Outline each Plasmodium ovale-infected red blood cell.
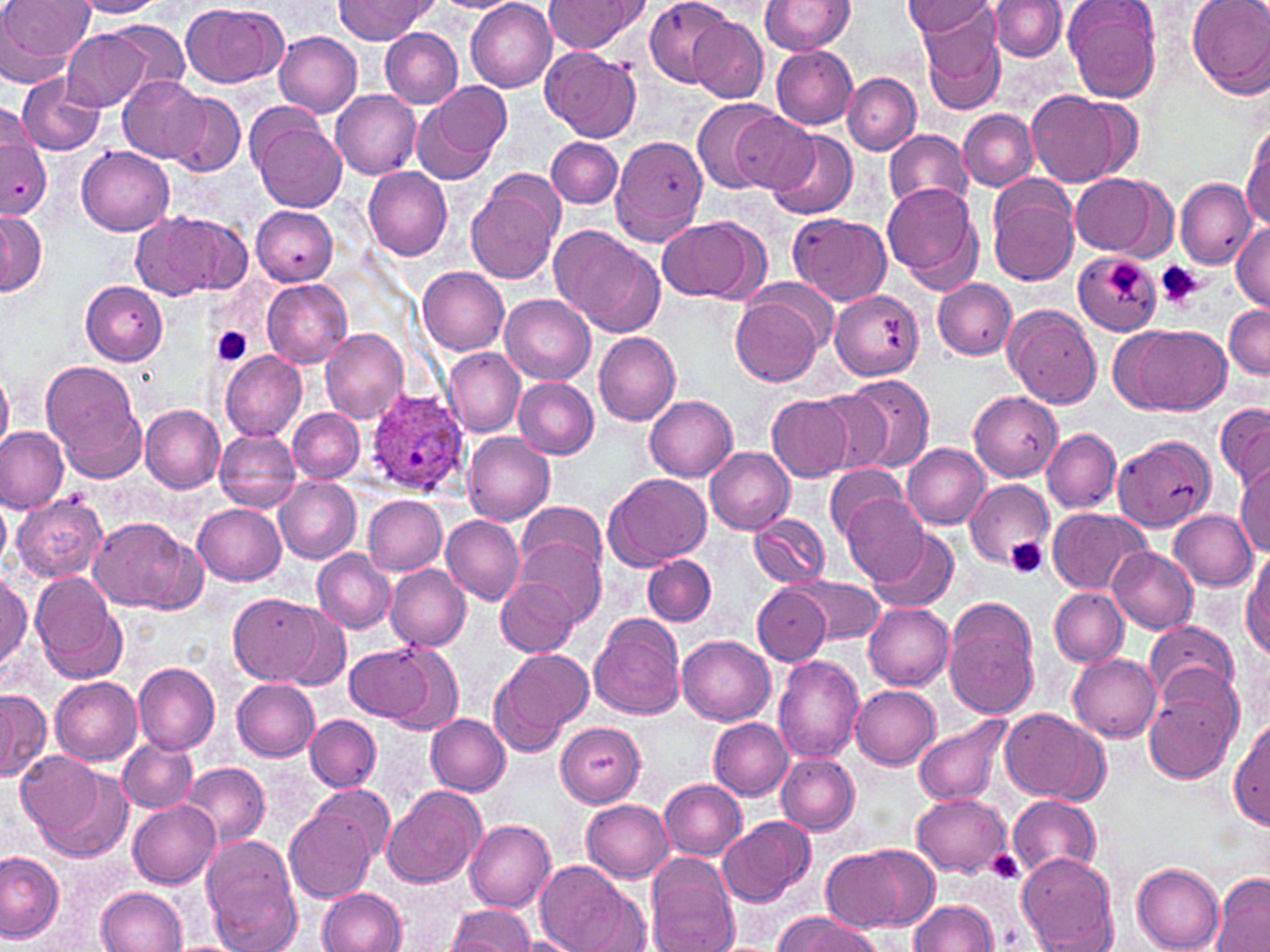
Approximate bounding boxes as [x1, y1, x2, y2] in pixels.
Plasmodium ovale-infected red blood cells: [367, 390, 470, 494].

slide-level diagnosis = Plasmodium ovale
stain = May-Grünwald-Giemsa
platelet locations = approximate bounding boxes as [x1, y1, x2, y2] in pixels: [1106, 261, 1146, 304], [1156, 261, 1204, 311], [212, 326, 253, 367], [1007, 538, 1048, 580], [987, 850, 1025, 884]
preparation = thin blood film
magnification = 1000x
field of view = one of a larger specimen
modality = optical microscopy
image size = 1270×952 pixels
uninfected red blood cell locations = approximate bounding boxes as [x1, y1, x2, y2] in pixels: [0, 0, 93, 83], [70, 0, 169, 18], [337, 0, 436, 42], [437, 0, 519, 13], [467, 0, 557, 91], [544, 0, 642, 55], [645, 0, 735, 87], [762, 0, 854, 53], [1064, 0, 1163, 102], [1187, 0, 1270, 98], [905, 1, 995, 38], [987, 1, 1066, 61], [181, 2, 286, 86], [915, 4, 1006, 109], [689, 16, 767, 101], [96, 20, 192, 104], [61, 27, 160, 112], [380, 29, 461, 108], [276, 33, 363, 117], [540, 47, 641, 142], [771, 47, 858, 129], [843, 73, 920, 154], [17, 74, 104, 155], [119, 76, 209, 164], [413, 82, 510, 183], [1025, 89, 1132, 187], [332, 90, 422, 179], [166, 92, 245, 177], [692, 97, 780, 193], [958, 109, 1037, 190], [730, 113, 819, 195], [251, 118, 346, 213], [0, 124, 50, 218], [1243, 126, 1270, 230], [884, 129, 973, 212], [769, 130, 857, 219], [609, 136, 707, 245], [546, 137, 622, 208], [77, 146, 174, 235], [363, 167, 453, 261], [1069, 173, 1164, 256], [466, 174, 562, 284], [1176, 178, 1256, 270], [987, 179, 1078, 286], [882, 184, 981, 285], [251, 207, 336, 285], [0, 208, 46, 295], [133, 211, 251, 299], [789, 213, 891, 306], [659, 218, 760, 303], [1231, 222, 1270, 309], [551, 225, 649, 329], [1074, 253, 1162, 334], [418, 267, 509, 354], [263, 279, 352, 368], [933, 279, 1017, 359], [81, 281, 168, 365], [830, 291, 923, 380], [501, 294, 594, 384], [731, 295, 824, 386], [1223, 304, 1270, 378], [1006, 306, 1103, 408], [1120, 324, 1224, 416], [320, 327, 408, 423], [594, 331, 681, 424], [443, 348, 524, 437], [220, 349, 306, 441], [43, 361, 143, 474], [0, 370, 13, 453], [840, 374, 935, 474], [514, 378, 598, 459], [970, 391, 1060, 481], [814, 392, 892, 474], [645, 396, 737, 481], [766, 396, 853, 482], [1215, 403, 1270, 492], [141, 405, 225, 493], [289, 409, 364, 482], [0, 425, 69, 512], [1043, 428, 1120, 513], [215, 430, 302, 513], [463, 431, 555, 524], [1115, 434, 1216, 533], [903, 443, 991, 528], [705, 446, 796, 532], [824, 464, 906, 537], [1234, 464, 1270, 555], [605, 472, 710, 569], [276, 476, 361, 563], [965, 479, 1054, 572], [841, 493, 928, 583], [364, 494, 448, 576], [14, 496, 107, 582], [0, 497, 11, 569], [517, 501, 606, 586], [193, 504, 286, 586], [1046, 508, 1148, 595], [1170, 509, 1257, 590], [750, 513, 829, 587], [87, 516, 201, 613], [442, 516, 524, 605], [869, 526, 961, 613], [517, 536, 605, 626], [1109, 546, 1197, 635], [313, 549, 396, 634], [1244, 550, 1270, 662], [643, 554, 715, 627], [386, 562, 470, 650], [31, 572, 126, 683], [0, 574, 31, 676], [787, 574, 887, 645], [497, 578, 576, 657], [753, 584, 832, 666], [1051, 588, 1128, 666], [229, 592, 329, 684], [944, 598, 1041, 720], [864, 602, 954, 689], [278, 605, 349, 691], [589, 614, 687, 719], [1145, 621, 1238, 707], [677, 633, 775, 723], [376, 644, 464, 736], [345, 646, 434, 722], [489, 648, 592, 755], [1068, 653, 1162, 740], [772, 654, 863, 764], [134, 662, 220, 754], [52, 677, 143, 766], [233, 678, 319, 761], [1145, 681, 1240, 784], [850, 682, 941, 769], [0, 690, 50, 782], [1000, 709, 1098, 802], [306, 714, 381, 792], [426, 714, 511, 795], [914, 717, 1010, 806], [709, 718, 793, 800], [1231, 718, 1269, 828], [555, 719, 646, 807], [119, 737, 196, 813], [17, 750, 104, 841], [775, 753, 860, 834], [179, 761, 270, 849], [40, 770, 131, 862], [659, 778, 748, 861], [312, 784, 394, 861], [383, 784, 487, 889], [913, 794, 1011, 877], [1008, 795, 1101, 879], [582, 797, 674, 882], [128, 799, 221, 888], [284, 807, 375, 902], [718, 817, 812, 906], [466, 821, 555, 911], [202, 837, 301, 951], [984, 844, 1032, 886], [859, 845, 941, 928], [1, 850, 62, 942], [822, 850, 904, 930], [1017, 851, 1119, 950], [646, 857, 738, 952], [537, 860, 628, 952], [1132, 863, 1225, 950], [1211, 873, 1269, 951], [568, 882, 652, 951], [96, 887, 187, 952], [317, 888, 406, 952], [910, 901, 999, 952], [446, 904, 535, 951], [773, 913, 873, 952], [517, 937, 576, 952]